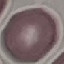

{
  "malaria_status": "uninfected",
  "preparation": "thin blood smear",
  "capture": "smartphone camera at the microscope eyepiece",
  "image_type": "cell patch, automatically extracted from a larger field of view and resized to 64 × 64 pixels",
  "stain": "Giemsa"
}